Describe the morphology of the red blood cells.
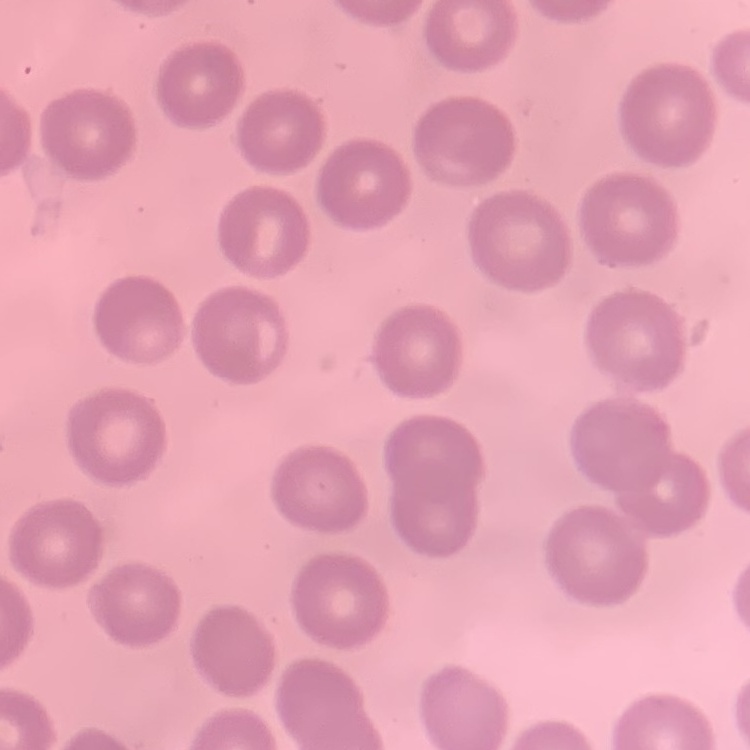

No rouleaux formation.

Thin blood smear. Field's or Giemsa stain. Square crop of a larger photomicrograph.